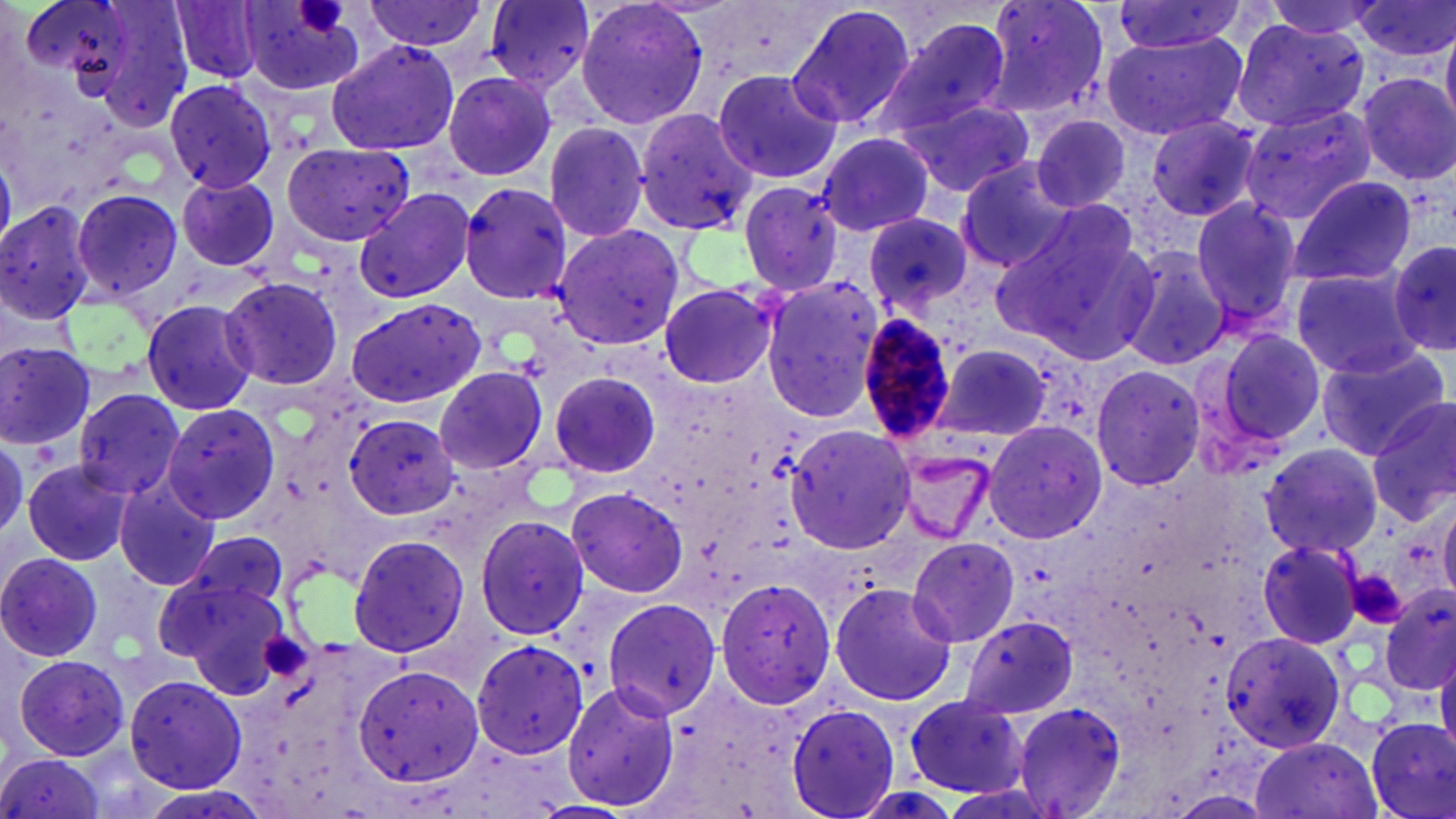
Approximate bounding boxes as (x1, y1, x2, y2) in pixels. Platelet locations: (296, 0, 345, 33), (1350, 570, 1413, 626), (263, 634, 314, 680). Plasmodium malariae-infected red blood cell locations: (855, 312, 958, 445). Uninfected red blood cell locations: (169, 0, 264, 83), (363, 0, 489, 56), (574, 0, 710, 133), (982, 0, 1110, 115), (1262, 0, 1391, 39), (1351, 0, 1455, 63), (240, 1, 366, 94), (484, 1, 595, 91), (786, 3, 918, 132), (1107, 3, 1247, 55), (1230, 15, 1369, 132), (875, 16, 1013, 138), (1441, 21, 1456, 126), (1102, 30, 1247, 140), (325, 39, 461, 157), (710, 67, 843, 186), (441, 70, 557, 182), (1357, 72, 1456, 185), (164, 78, 278, 194), (899, 99, 1037, 196), (1238, 103, 1376, 224), (634, 106, 758, 234), (1030, 115, 1133, 213), (1146, 115, 1263, 223), (542, 121, 651, 241), (818, 130, 934, 237), (282, 142, 419, 247), (956, 161, 1085, 272), (177, 174, 281, 271), (1289, 175, 1419, 287), (460, 181, 574, 304), (732, 181, 846, 296), (354, 187, 475, 303), (71, 188, 184, 303), (1189, 195, 1304, 333), (0, 199, 100, 327), (992, 212, 1155, 361), (863, 213, 974, 316), (551, 224, 687, 351), (1384, 239, 1454, 359), (1121, 244, 1230, 371), (1288, 266, 1425, 379), (220, 276, 343, 390), (759, 276, 884, 424), (658, 282, 778, 389), (140, 300, 261, 416), (344, 300, 486, 410), (1206, 326, 1327, 453), (0, 340, 100, 452), (933, 342, 1056, 447), (1316, 344, 1450, 458), (1090, 364, 1207, 492), (433, 366, 552, 477), (548, 367, 667, 481), (72, 387, 187, 499), (1368, 397, 1455, 527), (161, 405, 283, 525), (343, 414, 460, 521), (983, 419, 1106, 542), (785, 424, 916, 553), (0, 439, 28, 542), (1259, 443, 1386, 560), (889, 444, 1001, 546), (22, 460, 136, 568), (115, 480, 220, 591), (566, 486, 688, 598), (1438, 493, 1456, 600), (474, 514, 590, 642), (178, 531, 289, 621), (346, 534, 472, 659), (907, 537, 1019, 646), (1256, 540, 1368, 645), (0, 550, 104, 661), (159, 557, 292, 688), (714, 575, 834, 710), (829, 580, 957, 708), (1380, 593, 1455, 695), (603, 598, 725, 718), (959, 615, 1081, 719), (1220, 627, 1348, 757), (470, 639, 589, 759), (12, 654, 133, 762), (1436, 655, 1456, 759), (353, 663, 486, 792), (124, 675, 247, 791), (560, 679, 681, 815), (902, 694, 1026, 797), (1011, 701, 1128, 819), (786, 703, 902, 819), (1366, 717, 1456, 819), (1249, 736, 1383, 819), (0, 753, 113, 819). Slide-level diagnosis: Plasmodium malariae. Single field of view. May-Grünwald-Giemsa-stained preparation. Thin blood film. Image is 1456×819 pixels. Optical microscopy. 1000x magnification.